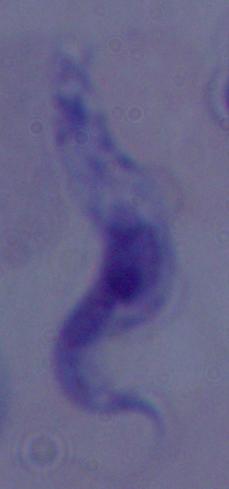

Summary:
  - Magnification: 1000x
  - Modality: photomicrograph
  - Identification: trypanosome